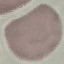

result = no malaria parasites detected
capture = smartphone camera at the microscope eyepiece
preparation = thin blood smear
stain = Giemsa
image type = automatically extracted cell patch, resized to 64 × 64 pixels